State which parasite is depicted.
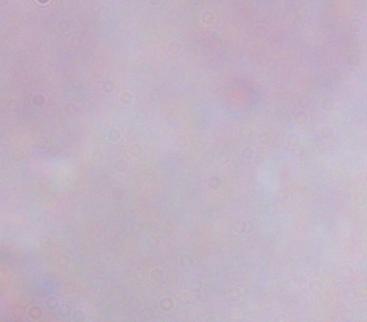
A trypanosome.

magnification = 1000x
modality = micrograph